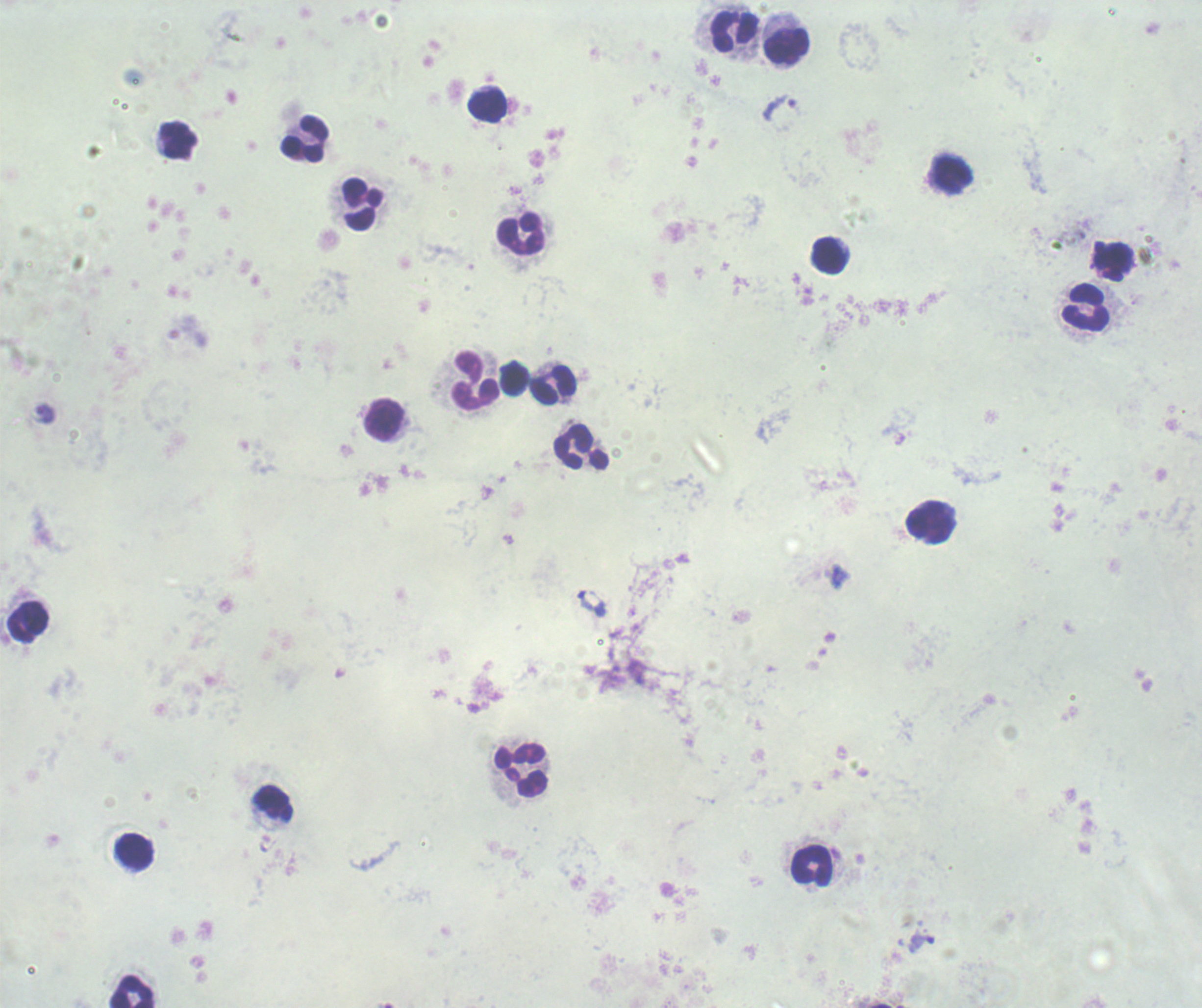 Approximate centers as {x, y} in pixels. Leukocyte locations: {735, 31}, {785, 46}, {487, 104}, {178, 139}, {304, 139}, {953, 174}, {362, 204}, {521, 233}, {829, 255}, {1087, 307}, {514, 379}, {476, 381}, {553, 384}, {384, 419}, {581, 447}, {931, 522}, {27, 621}, {521, 770}, {273, 803}, {134, 851}, {812, 866}, {133, 992}. Trophozoite locations: {778, 107}, {42, 414}, {921, 943}. Romanowsky stain. Result: Plasmodium parasites identified. Background quality: poor. Image is 1202×1008 pixels. One field from this slide. Previously used in a real diagnosis. Captured at 100x magnification. Thick blood film.